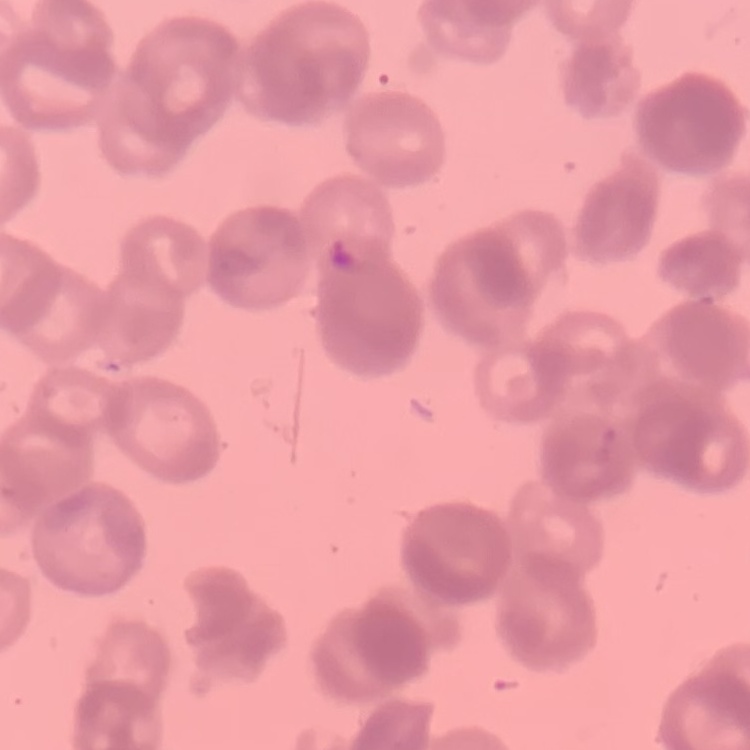
Summary:
  - Red blood cell morphology: rouleaux formation
  - Stain: Field's or Giemsa
  - Image type: one tile cut from a larger photomicrograph
  - Preparation: thin blood film